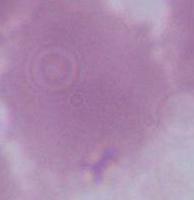
Summary:
  - Magnification: 1000x
  - Modality: micrograph
  - Identification: red blood cell